Assess the morphology of the red blood cells.
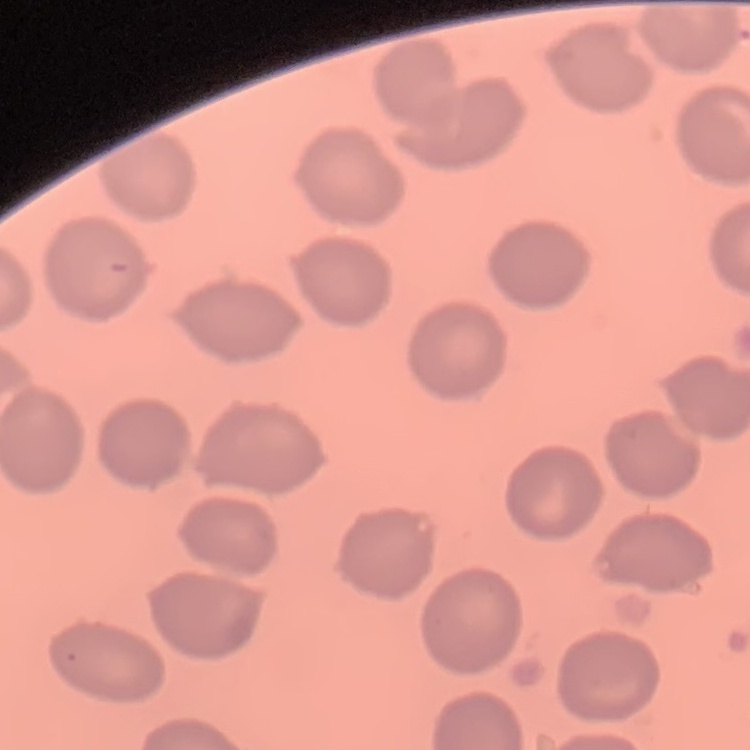
No rouleaux formation.

image type = square crop of a larger photomicrograph
preparation = thin blood smear
stain = Field's or Giemsa